Classify this cell by malaria status.
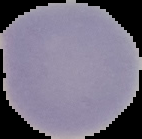
It is uninfected.

Cell region segmented out of the field of view; the surrounding area is masked to black. From a thin blood smear. Image is 142×139 pixels.